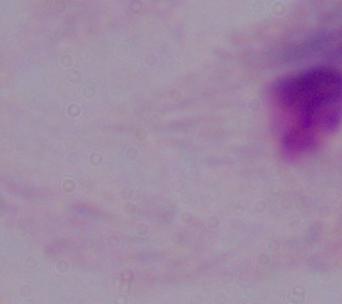

Summary:
  - Modality: micrograph
  - Magnification: 1000x
  - Identification: trichomonad